Locate every malaria parasite and every leukocyte.
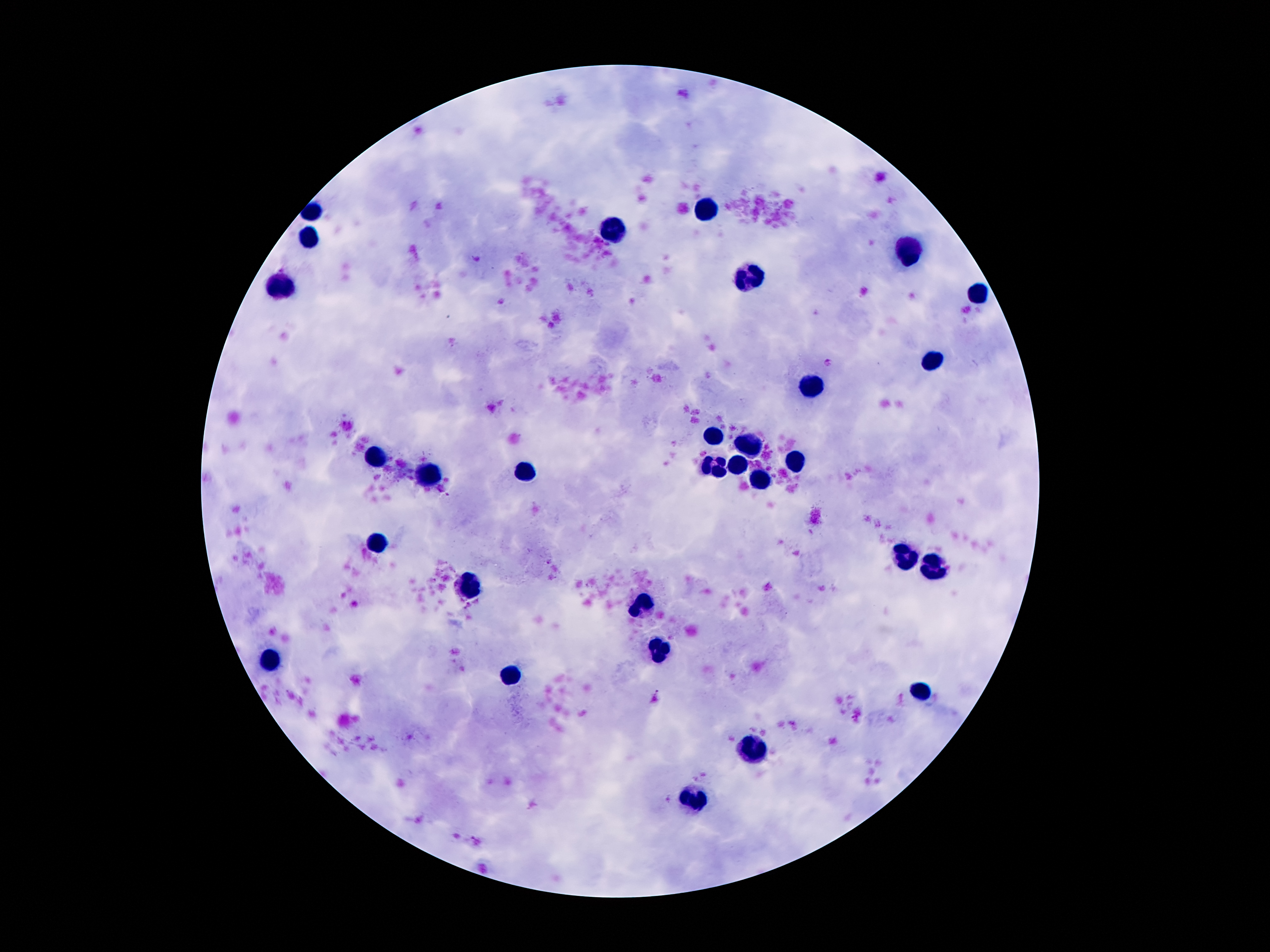
Approximate centers as [x, y] in pixels.
Malaria parasites: [478, 258], [500, 302], [828, 362], [657, 698].
Leukocytes: [709, 210], [314, 211], [617, 230], [307, 240], [908, 253], [750, 279], [283, 285], [976, 295], [933, 361], [810, 388], [713, 437], [750, 447], [375, 457], [795, 462], [736, 465], [523, 470], [713, 470], [434, 473], [762, 480], [373, 541], [904, 553], [935, 566], [469, 590], [641, 605], [658, 652], [268, 658], [512, 675], [920, 693], [754, 742], [695, 799].

Summary:
  - Patient malaria status: infected with Plasmodium falciparum
  - Stain: Giemsa
  - Preparation: thick blood film
  - Image size: 1270×952 pixels
  - Magnification: 100x
  - Field of view: one from this slide
  - Capture: smartphone camera through the microscope eyepiece